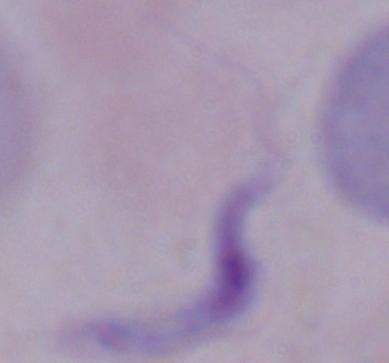

Summary:
  - Modality: micrograph
  - Identification: trypanosome
  - Magnification: 1000x